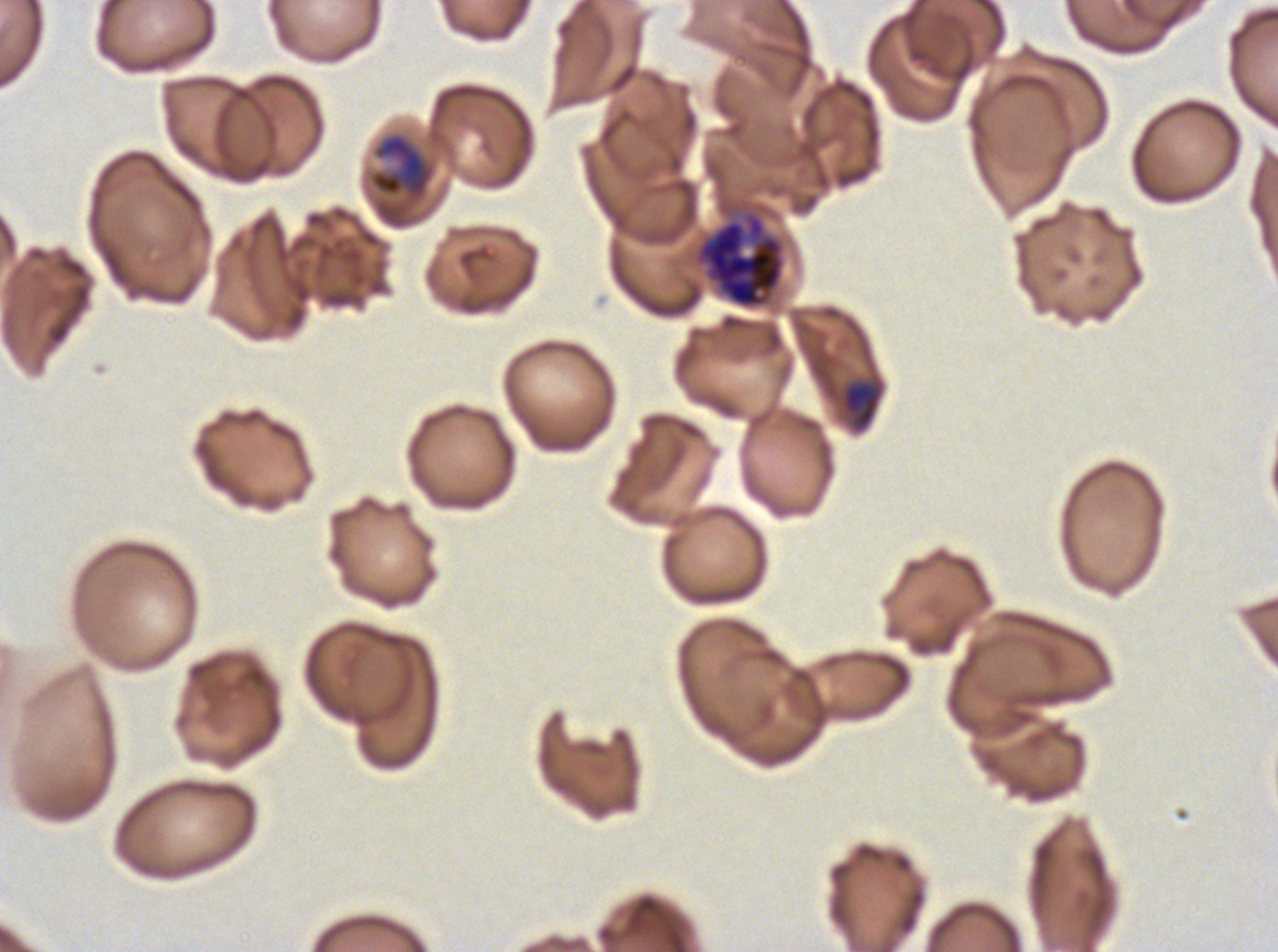

Approximate bounding boxes as (x1, y1, x2, y2) in pixels.
Summary:
  - Early schizont locations: (840, 379, 883, 433)
  - Late trophozoite locations: (371, 134, 433, 200)
  - Late schizont locations: (695, 212, 785, 309)
  - Field of view: one sub-image of a larger composite
  - Preparation: thin blood film
  - Image size: 1278×952 pixels
  - Stain: Giemsa
  - Specimen: Plasmodium falciparum cultured ex vivo for 24 to 48 hours, from a patient in The Gambia
  - Life-cycle stages observed: late trophozoite, early schizont, late schizont